Describe the morphology of the erythrocytes.
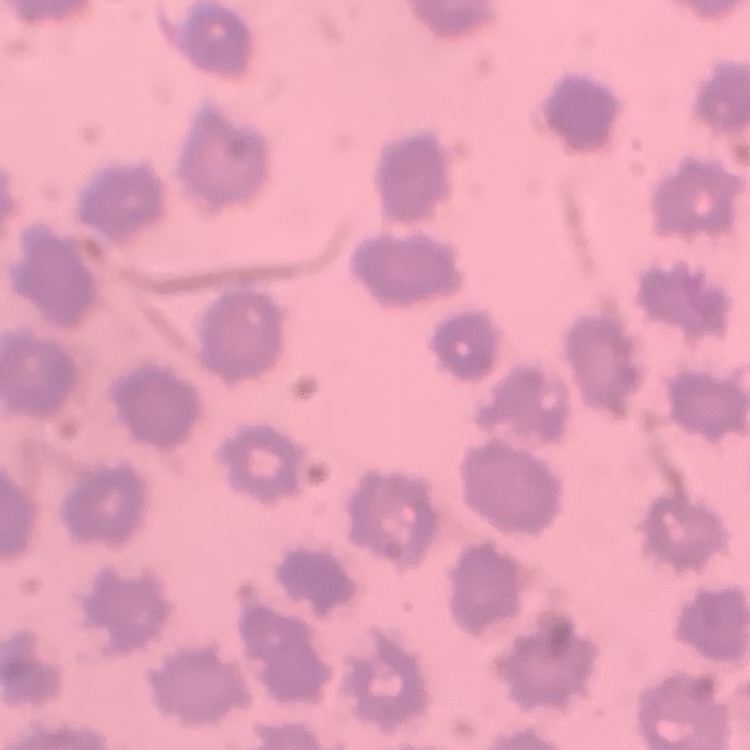
They show no rouleaux formation.

One tile cut from a larger photomicrograph. Field's or Giemsa stain. Thin blood smear.